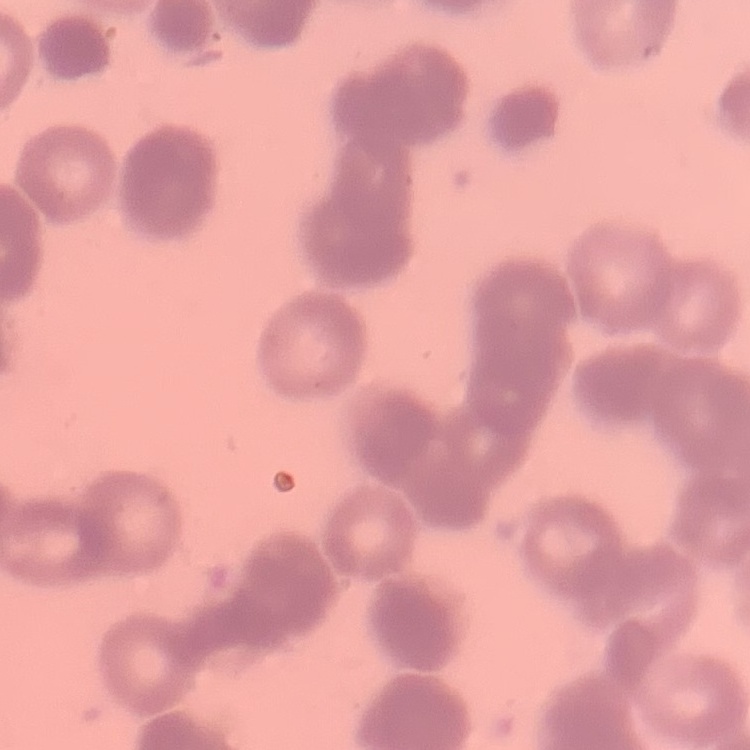

Summary:
  - Red blood cell morphology: rouleaux formation
  - Preparation: thin blood film
  - Image type: square crop of a larger photomicrograph
  - Stain: Field's or Giemsa